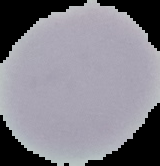
preparation = thin blood smear
image type = segmented cell region with the area outside set to black
malaria status = uninfected
image size = 160×166 pixels